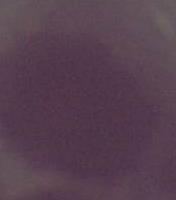
Captured at 1000x magnification. Photomicrograph. A red blood cell is seen.